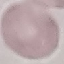

malaria_status: uninfected
image_type: automatically extracted cell patch, resized to 64 × 64 pixels
capture: smartphone camera at the microscope eyepiece
stain: Giemsa
preparation: thin blood film